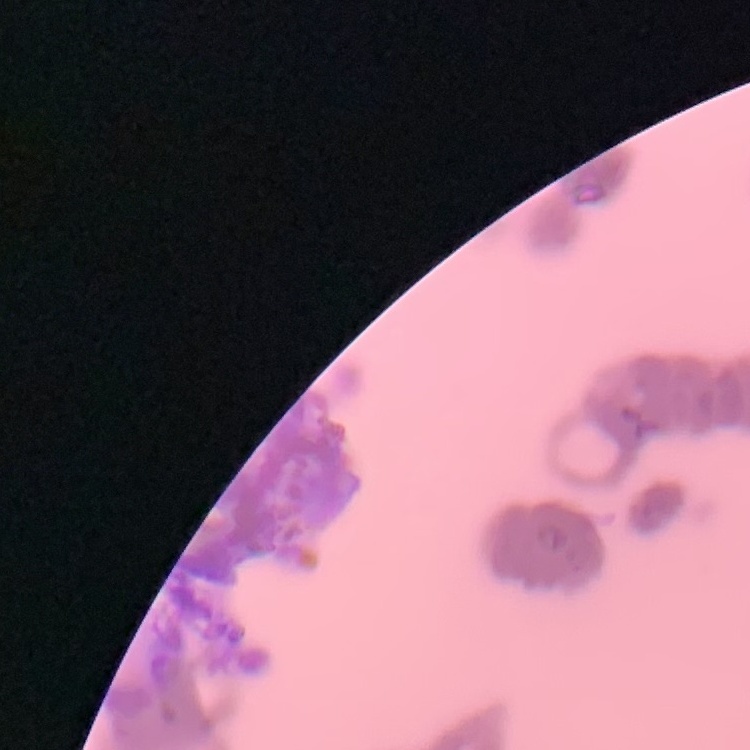
red blood cell morphology = rouleaux formation
image type = one tile cut from a larger photomicrograph
stain = Field's or Giemsa
preparation = thin blood film